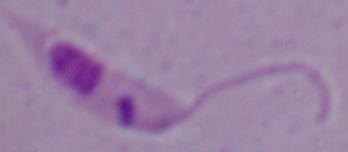

Summary:
  - Identification: Leishmania
  - Modality: micrograph
  - Magnification: 1000x